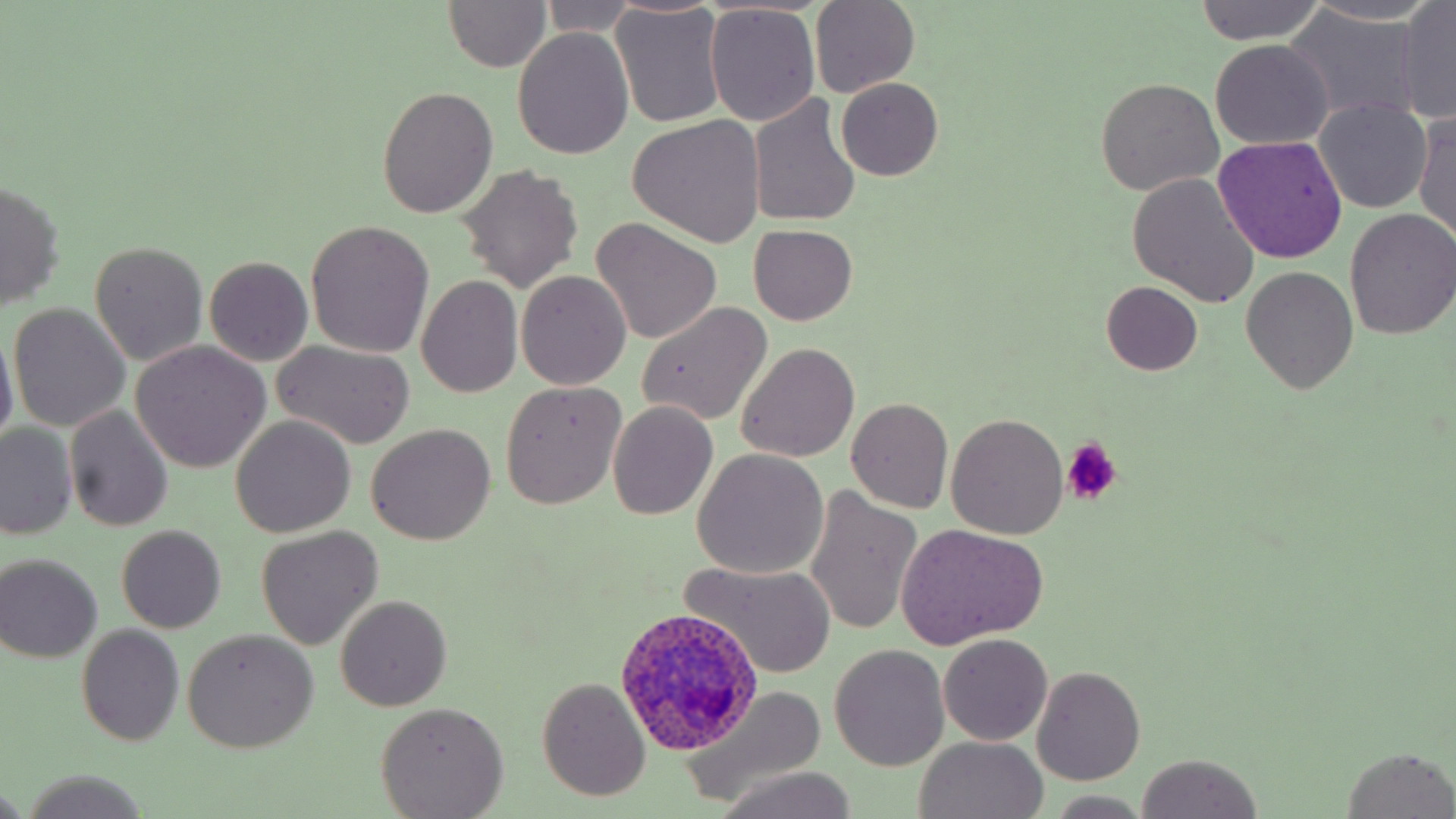

{
  "plasmodium_ovale_infected_red_blood_cell_locations": "approximate bounding boxes as [x1, y1, x2, y2] in pixels: [616, 603, 763, 756]",
  "slide_level_diagnosis": "Plasmodium ovale",
  "field_of_view": "one of a larger specimen",
  "modality": "optical microscopy",
  "preparation": "thin blood film",
  "stain": "May-Grünwald-Giemsa",
  "platelet_locations": "approximate bounding boxes as [x1, y1, x2, y2] in pixels: [1060, 441, 1121, 508]",
  "image_size": "1456×819 pixels",
  "magnification": "1000x",
  "uninfected_red_blood_cell_locations": "approximate bounding boxes as [x1, y1, x2, y2] in pixels: [1195, 0, 1328, 46], [442, 1, 553, 72], [536, 1, 644, 36], [809, 1, 920, 99], [1300, 1, 1441, 27], [1397, 1, 1456, 123], [704, 5, 820, 126], [610, 6, 728, 127], [1287, 8, 1424, 124], [513, 27, 636, 160], [1210, 40, 1333, 151], [836, 78, 943, 182], [1094, 79, 1223, 196], [376, 86, 498, 219], [749, 95, 861, 229], [1315, 100, 1432, 213], [1414, 106, 1455, 246], [629, 116, 767, 248], [1215, 137, 1348, 261], [458, 164, 583, 291], [1126, 174, 1260, 306], [1, 177, 67, 311], [1344, 208, 1456, 340], [591, 219, 723, 344], [306, 221, 435, 358], [750, 225, 857, 325], [91, 242, 208, 366], [205, 257, 313, 367], [1242, 267, 1359, 393], [516, 270, 632, 389], [417, 275, 524, 398], [1101, 281, 1203, 376], [637, 301, 772, 427], [8, 303, 131, 432], [1, 324, 20, 453], [130, 340, 269, 473], [274, 340, 415, 449], [736, 342, 860, 462], [500, 381, 626, 510], [847, 397, 953, 512], [608, 401, 717, 519], [64, 406, 174, 532], [946, 413, 1069, 538], [231, 414, 356, 536], [1, 423, 77, 541], [365, 425, 496, 546], [691, 448, 828, 578], [805, 486, 923, 637], [894, 523, 1049, 649], [118, 525, 225, 633], [257, 526, 382, 649], [0, 554, 103, 663], [683, 560, 836, 678], [335, 596, 452, 710], [76, 624, 184, 746], [182, 629, 318, 753], [939, 633, 1052, 745], [830, 644, 949, 771], [1032, 666, 1144, 784], [536, 678, 652, 801], [680, 684, 831, 805], [375, 702, 508, 818], [913, 737, 1050, 819], [1340, 747, 1456, 819], [1134, 753, 1262, 819], [713, 768, 863, 819], [15, 772, 154, 819], [0, 782, 28, 819], [1048, 793, 1151, 817]"
}